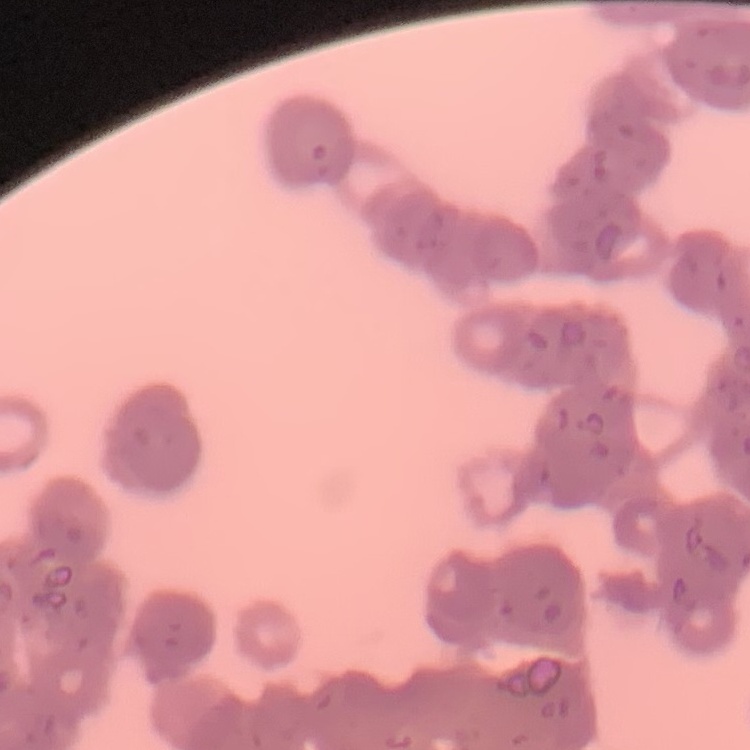
red blood cell morphology = rouleaux formation
preparation = thin peripheral smear
image type = square crop of a larger photomicrograph
stain = Field's or Giemsa